State which parasite is depicted.
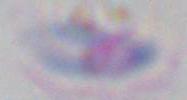
Toxoplasma gondii.

Summary:
  - Modality: micrograph
  - Magnification: 1000x